State the blood parasite species.
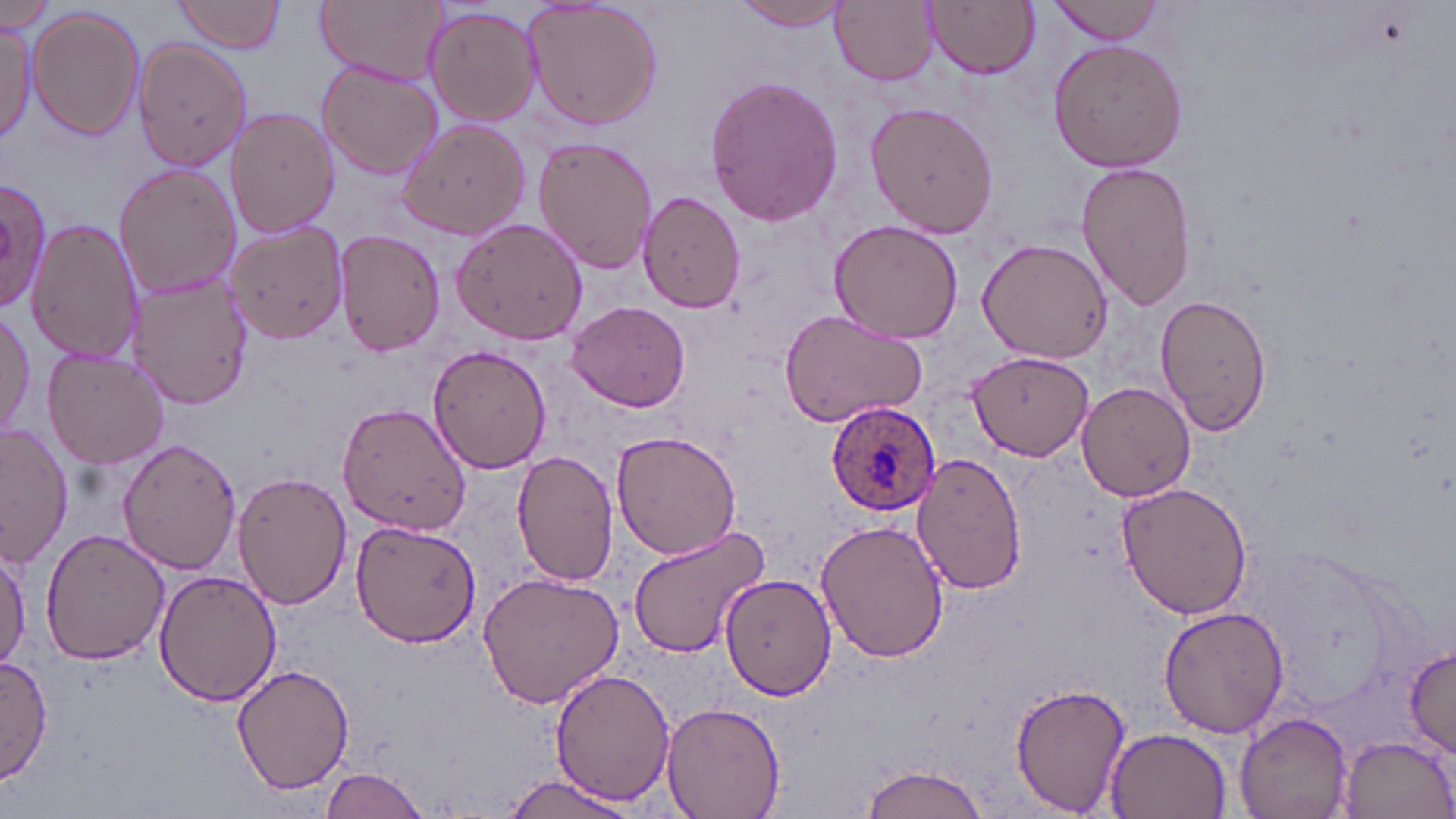

Plasmodium ovale.

Summary:
  - Coordinate format: approximate bounding boxes as named x1/y1/x2/y2 corners in pixels
  - Uninfected red blood cell locations: (x1=173, y1=0, x2=285, y2=53), (x1=316, y1=0, x2=446, y2=85), (x1=830, y1=0, x2=937, y2=87), (x1=1049, y1=0, x2=1168, y2=43), (x1=735, y1=1, x2=851, y2=31), (x1=924, y1=1, x2=1040, y2=79), (x1=520, y1=2, x2=664, y2=130), (x1=2, y1=4, x2=57, y2=35), (x1=421, y1=4, x2=543, y2=126), (x1=30, y1=7, x2=142, y2=140), (x1=0, y1=18, x2=37, y2=145), (x1=1047, y1=37, x2=1190, y2=174), (x1=134, y1=39, x2=255, y2=171), (x1=316, y1=60, x2=443, y2=178), (x1=704, y1=75, x2=845, y2=225), (x1=866, y1=101, x2=999, y2=238), (x1=225, y1=107, x2=338, y2=240), (x1=395, y1=117, x2=530, y2=239), (x1=532, y1=136, x2=660, y2=274), (x1=1077, y1=161, x2=1198, y2=311), (x1=113, y1=164, x2=241, y2=301), (x1=0, y1=177, x2=52, y2=310), (x1=638, y1=191, x2=748, y2=313), (x1=25, y1=216, x2=142, y2=369), (x1=450, y1=217, x2=588, y2=346), (x1=223, y1=218, x2=348, y2=347), (x1=830, y1=219, x2=963, y2=344), (x1=335, y1=230, x2=445, y2=356), (x1=976, y1=238, x2=1112, y2=364), (x1=127, y1=273, x2=251, y2=410), (x1=1154, y1=291, x2=1272, y2=435), (x1=567, y1=300, x2=693, y2=413), (x1=0, y1=308, x2=36, y2=444), (x1=778, y1=309, x2=927, y2=427), (x1=429, y1=344, x2=551, y2=474), (x1=43, y1=351, x2=169, y2=468), (x1=971, y1=352, x2=1092, y2=460), (x1=1077, y1=380, x2=1196, y2=501), (x1=336, y1=403, x2=473, y2=536), (x1=1, y1=424, x2=73, y2=568), (x1=611, y1=429, x2=745, y2=559), (x1=118, y1=438, x2=242, y2=576), (x1=510, y1=451, x2=618, y2=586), (x1=912, y1=453, x2=1028, y2=595), (x1=233, y1=471, x2=352, y2=611), (x1=1115, y1=480, x2=1254, y2=621), (x1=349, y1=518, x2=482, y2=647), (x1=816, y1=519, x2=951, y2=663), (x1=625, y1=524, x2=773, y2=663), (x1=40, y1=528, x2=168, y2=666), (x1=0, y1=535, x2=30, y2=670), (x1=152, y1=569, x2=279, y2=706), (x1=477, y1=570, x2=626, y2=709), (x1=719, y1=573, x2=836, y2=701), (x1=1158, y1=605, x2=1290, y2=738), (x1=1403, y1=641, x2=1456, y2=758), (x1=1, y1=656, x2=52, y2=784), (x1=232, y1=664, x2=357, y2=794), (x1=549, y1=667, x2=676, y2=805), (x1=1007, y1=680, x2=1129, y2=815), (x1=662, y1=700, x2=785, y2=819), (x1=1235, y1=713, x2=1353, y2=819), (x1=1104, y1=726, x2=1234, y2=819), (x1=1338, y1=734, x2=1455, y2=818), (x1=858, y1=763, x2=992, y2=819), (x1=320, y1=765, x2=430, y2=819), (x1=499, y1=771, x2=642, y2=818)
  - Plasmodium ovale-infected red blood cell locations: (x1=827, y1=402, x2=943, y2=517)
  - Stain: May-Grünwald-Giemsa
  - Preparation: thin blood film
  - Magnification: 1000x
  - Image size: 1456×819 pixels
  - Field of view: one of a larger specimen
  - Modality: light microscopy